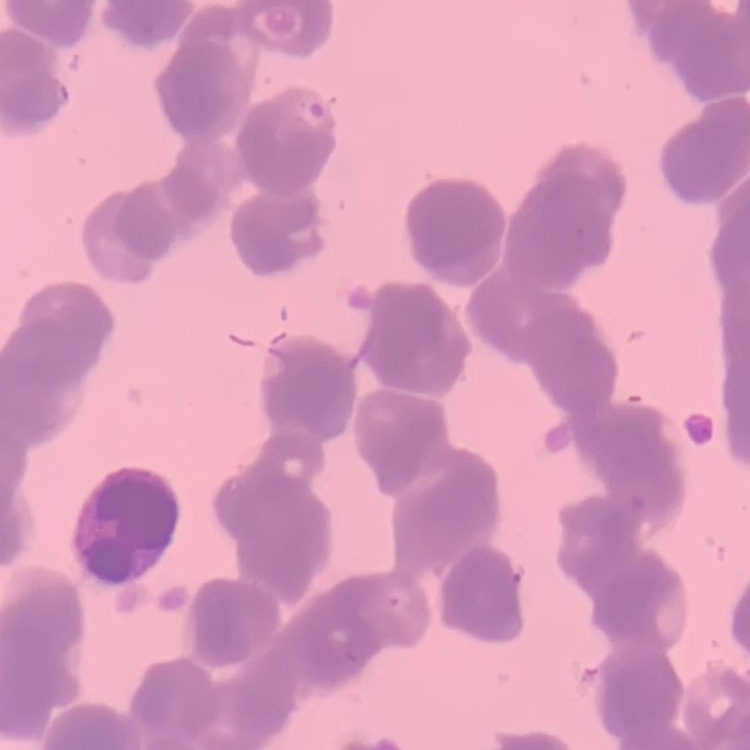

Summary:
  - Erythrocyte morphology: rouleaux formation
  - Stain: Field's or Giemsa
  - Preparation: thin blood smear
  - Image type: one tile cut from a larger photomicrograph